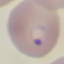

Summary:
  - Result: malaria parasites identified
  - Capture: smartphone camera at the microscope eyepiece
  - Image type: cell patch, automatically extracted from a larger field of view and resized to 64 × 64 pixels
  - Stain: Giemsa
  - Preparation: thin blood smear